Report the malaria status of this cell.
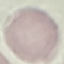
It is uninfected.

Summary:
  - Preparation: thin blood smear
  - Stain: Giemsa
  - Capture: smartphone camera at the microscope eyepiece
  - Image type: cell patch, automatically extracted from a larger field of view and resized to 64 × 64 pixels